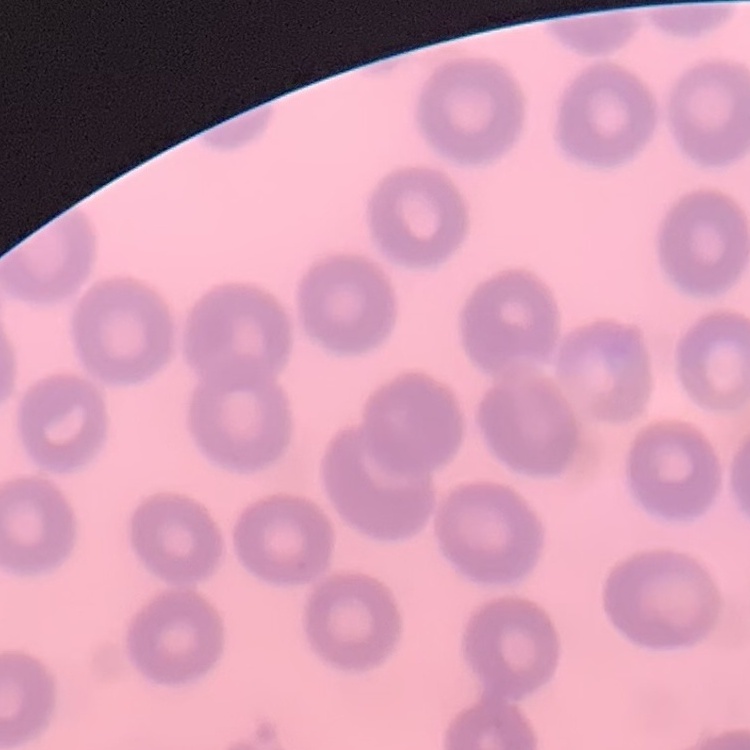

Summary:
  - Red blood cell morphology: no rouleaux formation
  - Preparation: thin blood smear
  - Image type: one tile cut from a larger photomicrograph
  - Stain: Field's or Giemsa